Name the blood parasite species.
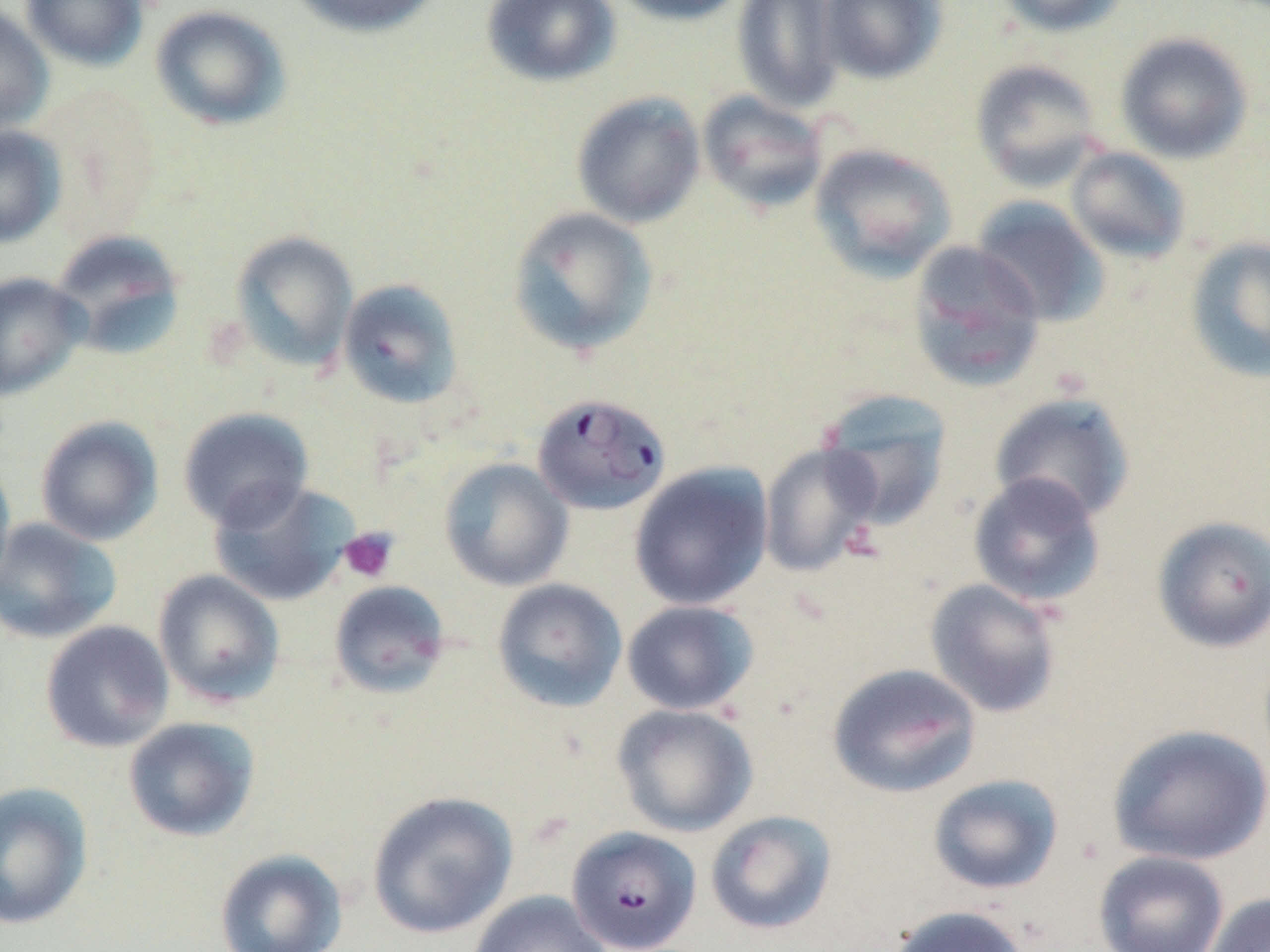
Plasmodium falciparum.

stain: May-Grünwald-Giemsa
modality: light microscopy
field_of_view: single
preparation: thin blood smear
magnification: 1000x
uninfected_red_blood_cell_locations: 'approximate bounding boxes as (x1, y1, x2, y2) in pixels: (21, 0, 149, 71), (287, 0, 444, 39), (482, 0, 621, 87), (607, 0, 750, 26), (731, 0, 847, 113), (818, 0, 949, 84), (993, 0, 1130, 38), (0, 5, 54, 135), (150, 5, 291, 131), (1115, 31, 1254, 164), (970, 59, 1104, 190), (571, 91, 706, 228), (697, 91, 829, 215), (0, 126, 66, 248), (809, 143, 957, 282), (1066, 146, 1192, 263), (971, 196, 1110, 327), (507, 206, 659, 357), (50, 229, 186, 361), (230, 231, 359, 372), (1184, 235, 1270, 384), (906, 241, 1046, 392), (0, 272, 89, 401), (337, 278, 464, 410), (816, 389, 954, 530), (989, 391, 1137, 523), (178, 407, 314, 531), (35, 415, 164, 546), (758, 442, 883, 578), (0, 455, 16, 595), (439, 457, 573, 591), (629, 461, 773, 610), (967, 472, 1106, 608), (208, 480, 358, 607), (1151, 515, 1270, 654), (0, 517, 121, 644), (153, 569, 285, 708), (491, 578, 628, 712), (924, 578, 1064, 719), (328, 579, 451, 698), (621, 600, 759, 716), (40, 620, 174, 753), (826, 662, 982, 798), (612, 704, 759, 837), (123, 717, 260, 842), (1107, 723, 1270, 866), (927, 773, 1064, 895), (0, 781, 94, 930), (366, 790, 519, 940), (705, 810, 837, 936), (214, 848, 348, 952), (1093, 850, 1230, 952), (468, 890, 611, 952), (1204, 893, 1270, 952), (885, 904, 1034, 952)'
platelet_locations: 'approximate bounding boxes as (x1, y1, x2, y2) in pixels: (840, 522, 886, 563), (339, 527, 399, 583)'
plasmodium_falciparum_infected_red_blood_cell_locations: 'approximate bounding boxes as (x1, y1, x2, y2) in pixels: (532, 392, 672, 516), (567, 826, 701, 952)'
image_size: 1270×952 pixels